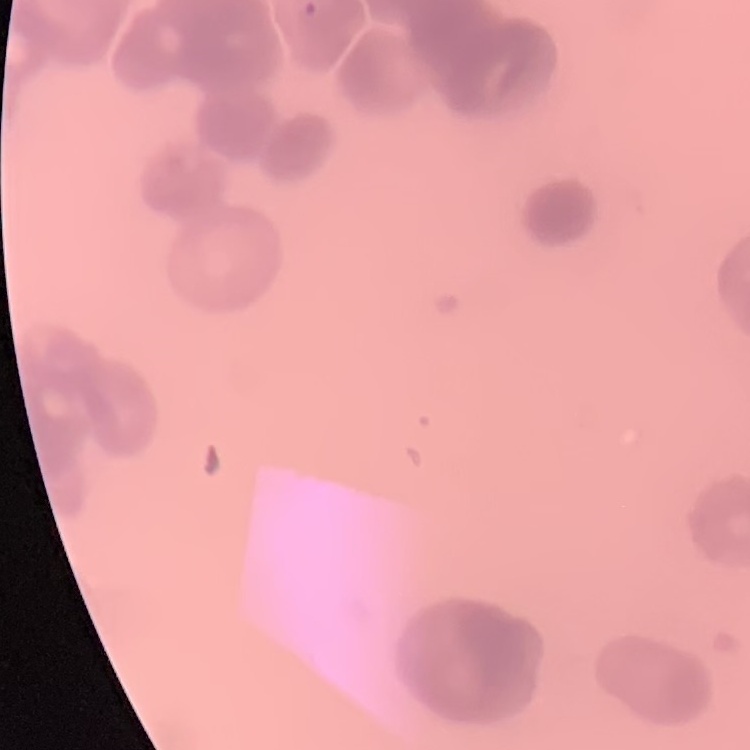

The red blood cells show rouleaux formation. One tile cut from a larger photomicrograph. Thin blood smear. Stained with either Field's or Giemsa.